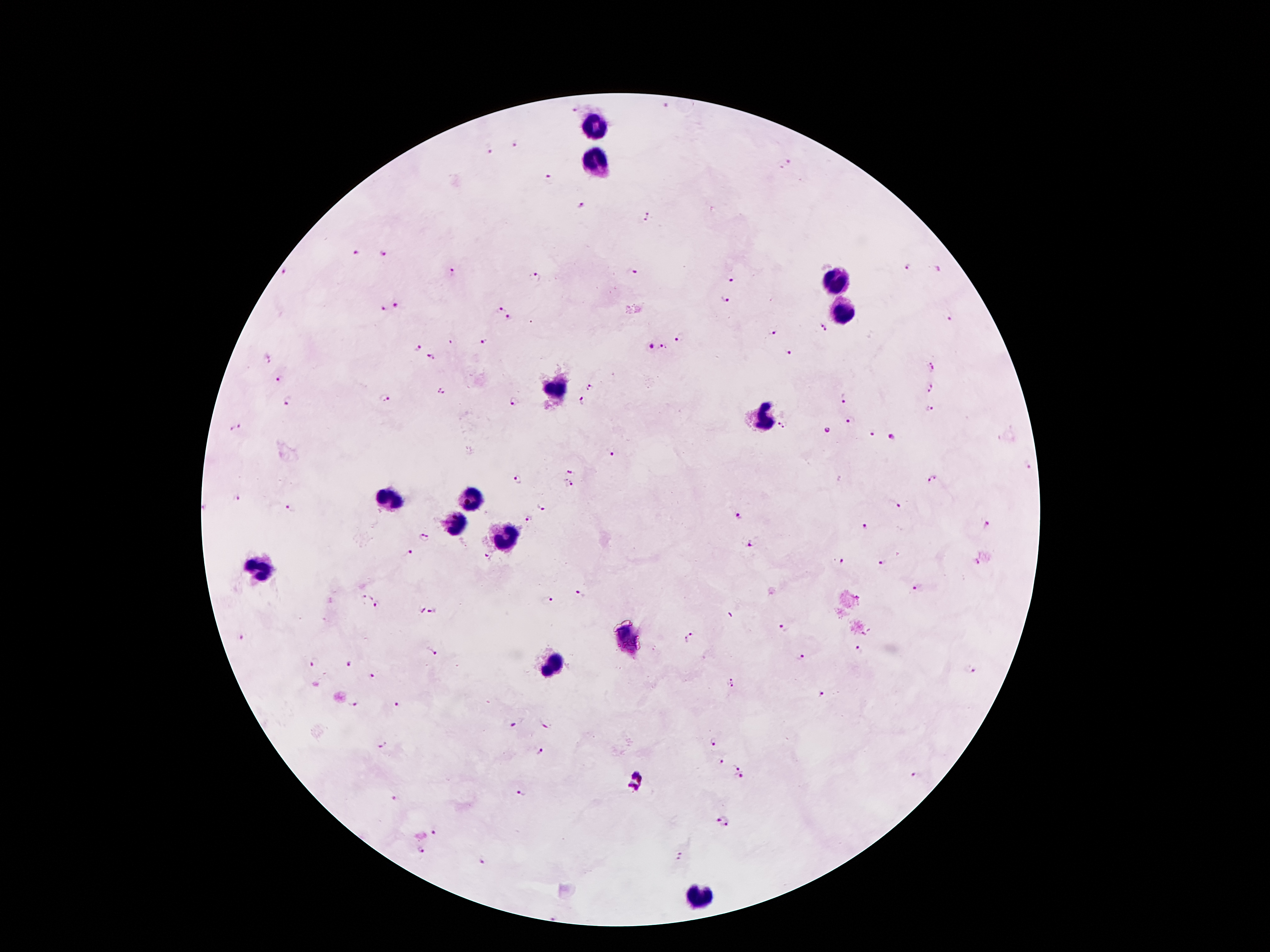

Approximate object centers, in pixels from the top-left corner. Leukocyte locations: (x=593, y=127), (x=595, y=164), (x=840, y=282), (x=842, y=309), (x=557, y=393), (x=761, y=421), (x=477, y=496), (x=391, y=498), (x=454, y=522), (x=507, y=538), (x=263, y=570), (x=626, y=639), (x=551, y=666), (x=696, y=893). Plasmodium parasite locations: (x=574, y=110), (x=516, y=143), (x=490, y=150), (x=784, y=165), (x=546, y=179), (x=581, y=203), (x=647, y=217), (x=385, y=251), (x=358, y=255), (x=906, y=266), (x=638, y=270), (x=938, y=270), (x=452, y=271), (x=286, y=274), (x=536, y=278), (x=731, y=279), (x=726, y=298), (x=396, y=304), (x=380, y=309), (x=499, y=309), (x=510, y=317), (x=949, y=318), (x=822, y=326), (x=772, y=332), (x=681, y=336), (x=451, y=341), (x=484, y=344), (x=650, y=347), (x=417, y=348), (x=665, y=348), (x=789, y=354), (x=266, y=357), (x=432, y=357), (x=932, y=366), (x=277, y=377), (x=592, y=387), (x=442, y=388), (x=929, y=390), (x=845, y=396), (x=386, y=397), (x=288, y=401), (x=514, y=401), (x=583, y=401), (x=931, y=410), (x=852, y=420), (x=783, y=425), (x=237, y=428), (x=828, y=430), (x=873, y=432), (x=892, y=435), (x=613, y=452), (x=1026, y=465), (x=572, y=469), (x=932, y=479), (x=518, y=480), (x=569, y=486), (x=236, y=498), (x=896, y=506), (x=544, y=507), (x=288, y=509), (x=738, y=515), (x=528, y=519), (x=987, y=525), (x=864, y=527), (x=424, y=536), (x=751, y=544), (x=407, y=554), (x=486, y=557), (x=841, y=561), (x=880, y=562), (x=976, y=562), (x=919, y=589), (x=581, y=593), (x=365, y=598), (x=550, y=599), (x=377, y=604), (x=419, y=610), (x=433, y=610), (x=783, y=627), (x=241, y=637), (x=686, y=638), (x=428, y=648), (x=857, y=651), (x=800, y=656), (x=315, y=663), (x=349, y=664), (x=970, y=670), (x=373, y=674), (x=732, y=683), (x=820, y=693), (x=393, y=704), (x=352, y=705), (x=512, y=722), (x=546, y=723), (x=714, y=741), (x=382, y=743), (x=539, y=749), (x=724, y=756), (x=737, y=767), (x=917, y=776), (x=742, y=779), (x=636, y=782), (x=518, y=791), (x=395, y=799), (x=722, y=819), (x=435, y=832), (x=420, y=852), (x=679, y=856), (x=482, y=862). Single field of view. Patient malaria status: positive for Plasmodium falciparum. Thick peripheral-blood smear. Image is 1270×952 pixels. Smartphone photograph taken through the microscope eyepiece. 100x magnification. Giemsa-stained preparation.